Assess this cell for malaria.
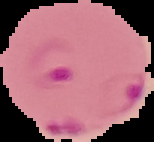

It is parasitized.

Summary:
  - Image type: segmented cell region on a black background
  - Preparation: thin blood film
  - Image size: 154×142 pixels